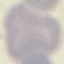

Summary:
  - Result: no malaria parasites detected
  - Preparation: thin blood film
  - Image type: automatically extracted cell patch, resized to 64 × 64 pixels
  - Stain: Giemsa
  - Capture: smartphone camera at the microscope eyepiece